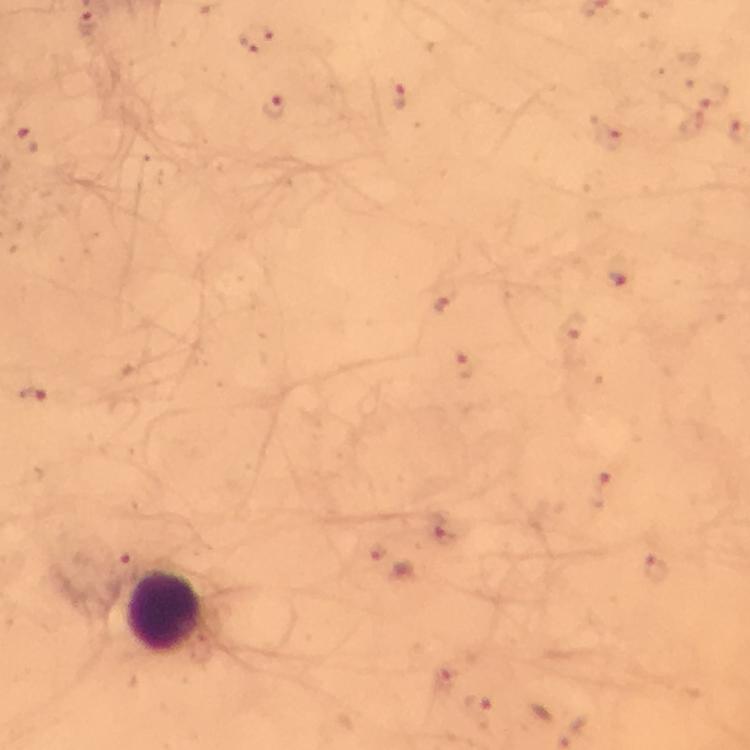

malaria_parasite_locations: 'approximate centers as (x, y) in pixels: (88, 23), (713, 95), (397, 98), (273, 105), (24, 140), (620, 271), (33, 395), (656, 569)'
magnification: 100x
context: from a diagnostic examination for malaria
cropped_from: one field of view
image_size: 750×750 pixels
preparation: thick blood smear
leukocyte_locations: 'approximate centers as (x, y) in pixels: (165, 612)'
capture: smartphone mounted on the microscope
stain: Giemsa
immersion_oil: used